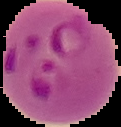

Image is 121×127 pixels. Result: malaria parasites identified. From a thin blood smear. Segmented cell region on a black background.